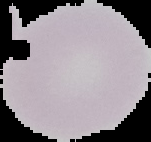
Image is 151×142 pixels. Segmented cell region on a black background. From a thin blood film. Result: no malaria parasites seen.